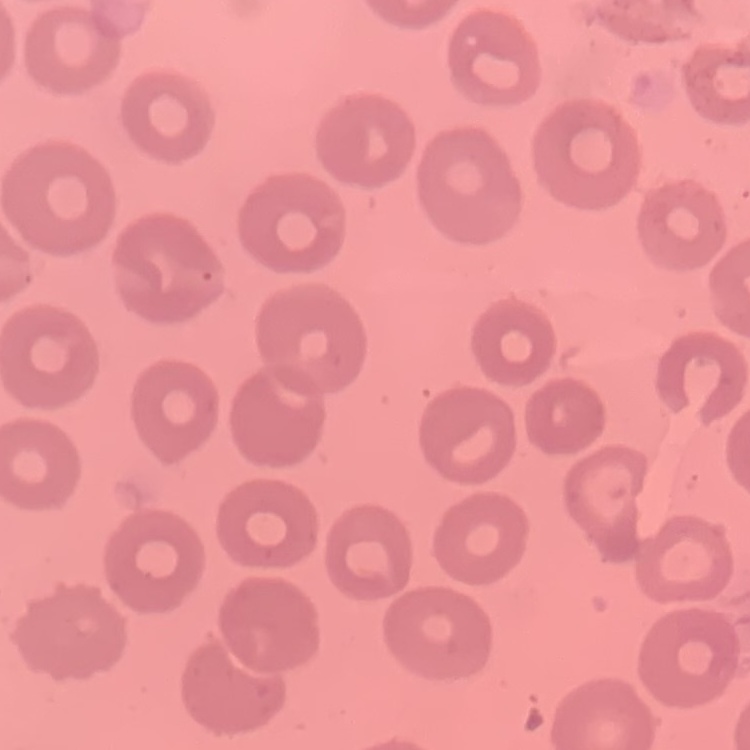
Summary:
  - Erythrocyte morphology: no rouleaux formation
  - Preparation: thin blood film
  - Stain: Field's or Giemsa
  - Image type: one tile cut from a larger photomicrograph